Report the malaria status of this cell.
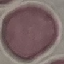
It is uninfected.

Photographed with a smartphone camera at the microscope eyepiece. Giemsa stain. Thin smear of blood. Automatically extracted cell patch, resized to 64 × 64 pixels.